Assess this cell for malaria.
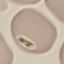
It is uninfected.

Summary:
  - Preparation: thin blood smear
  - Image type: cell patch, automatically extracted from a larger field of view and resized to 64 × 64 pixels
  - Stain: Giemsa
  - Capture: smartphone camera at the microscope eyepiece